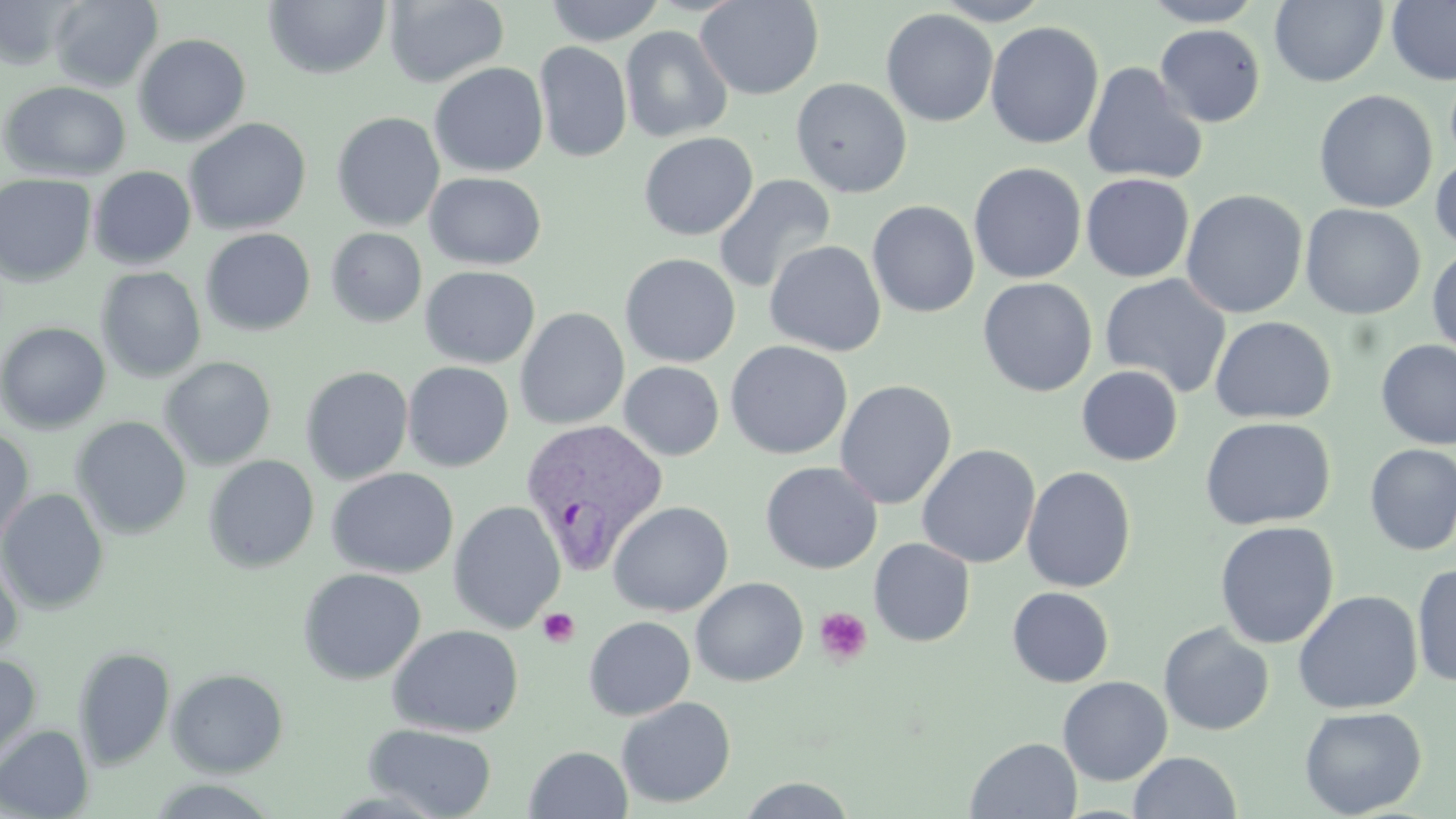
Summary:
  - Coordinate format: approximate bounding boxes as named x1/y1/x2/y2 corners in pixels
  - Plasmodium vivax-infected red blood cell locations: (x1=520, y1=418, x2=670, y2=574)
  - Uninfected red blood cell locations: (x1=49, y1=0, x2=163, y2=92), (x1=544, y1=0, x2=666, y2=46), (x1=694, y1=0, x2=824, y2=100), (x1=932, y1=0, x2=1052, y2=25), (x1=1140, y1=0, x2=1266, y2=26), (x1=1270, y1=0, x2=1388, y2=87), (x1=1386, y1=0, x2=1456, y2=86), (x1=0, y1=1, x2=80, y2=70), (x1=264, y1=1, x2=391, y2=79), (x1=384, y1=1, x2=509, y2=88), (x1=881, y1=8, x2=998, y2=127), (x1=985, y1=21, x2=1104, y2=150), (x1=981, y1=22, x2=1094, y2=285), (x1=1154, y1=24, x2=1266, y2=127), (x1=620, y1=25, x2=733, y2=143), (x1=133, y1=33, x2=252, y2=146), (x1=534, y1=41, x2=632, y2=162), (x1=1082, y1=61, x2=1208, y2=185), (x1=429, y1=62, x2=549, y2=177), (x1=790, y1=77, x2=912, y2=199), (x1=1, y1=80, x2=131, y2=182), (x1=1314, y1=89, x2=1437, y2=213), (x1=331, y1=112, x2=445, y2=232), (x1=184, y1=117, x2=312, y2=236), (x1=639, y1=132, x2=758, y2=240), (x1=1430, y1=151, x2=1456, y2=257), (x1=968, y1=162, x2=1087, y2=284), (x1=88, y1=166, x2=196, y2=270), (x1=0, y1=172, x2=97, y2=287), (x1=424, y1=172, x2=546, y2=270), (x1=1081, y1=172, x2=1194, y2=282), (x1=712, y1=174, x2=837, y2=294), (x1=1180, y1=189, x2=1308, y2=319), (x1=867, y1=200, x2=980, y2=317), (x1=1300, y1=203, x2=1426, y2=319), (x1=325, y1=227, x2=427, y2=327), (x1=201, y1=228, x2=316, y2=336), (x1=764, y1=240, x2=886, y2=357), (x1=1427, y1=245, x2=1456, y2=361), (x1=620, y1=253, x2=741, y2=368), (x1=420, y1=266, x2=540, y2=368), (x1=96, y1=267, x2=206, y2=382), (x1=1099, y1=274, x2=1231, y2=399), (x1=977, y1=278, x2=1097, y2=397), (x1=514, y1=307, x2=630, y2=430), (x1=1210, y1=315, x2=1336, y2=424), (x1=0, y1=321, x2=111, y2=434), (x1=1374, y1=339, x2=1456, y2=449), (x1=725, y1=340, x2=853, y2=460), (x1=158, y1=356, x2=277, y2=470), (x1=402, y1=361, x2=514, y2=472), (x1=619, y1=361, x2=725, y2=461), (x1=1076, y1=365, x2=1183, y2=466), (x1=300, y1=366, x2=413, y2=485), (x1=834, y1=380, x2=957, y2=509), (x1=71, y1=416, x2=192, y2=539), (x1=1199, y1=416, x2=1336, y2=531), (x1=0, y1=427, x2=34, y2=545), (x1=917, y1=444, x2=1040, y2=568), (x1=1364, y1=444, x2=1456, y2=556), (x1=203, y1=455, x2=319, y2=574), (x1=760, y1=461, x2=882, y2=574), (x1=1022, y1=466, x2=1137, y2=593), (x1=326, y1=467, x2=459, y2=579), (x1=0, y1=488, x2=109, y2=614), (x1=448, y1=501, x2=566, y2=634), (x1=608, y1=501, x2=733, y2=617), (x1=1215, y1=520, x2=1339, y2=650), (x1=869, y1=538, x2=976, y2=647), (x1=0, y1=548, x2=23, y2=663), (x1=1412, y1=562, x2=1456, y2=688), (x1=298, y1=567, x2=426, y2=685), (x1=690, y1=577, x2=809, y2=687), (x1=1007, y1=586, x2=1115, y2=688), (x1=1293, y1=589, x2=1423, y2=714), (x1=584, y1=616, x2=696, y2=720), (x1=1158, y1=622, x2=1274, y2=736), (x1=387, y1=624, x2=524, y2=737), (x1=73, y1=646, x2=176, y2=770), (x1=0, y1=654, x2=41, y2=764), (x1=167, y1=668, x2=289, y2=777), (x1=1058, y1=676, x2=1173, y2=785), (x1=616, y1=696, x2=736, y2=808), (x1=1299, y1=705, x2=1427, y2=818), (x1=364, y1=723, x2=498, y2=819), (x1=0, y1=724, x2=94, y2=818), (x1=965, y1=737, x2=1082, y2=818), (x1=524, y1=746, x2=633, y2=819), (x1=1128, y1=751, x2=1241, y2=819), (x1=145, y1=777, x2=283, y2=818), (x1=736, y1=777, x2=859, y2=818)
  - Platelet locations: (x1=814, y1=607, x2=872, y2=666), (x1=538, y1=608, x2=580, y2=647)
  - Slide-level diagnosis: Plasmodium vivax
  - Field of view: one of a larger specimen
  - Modality: light microscopy
  - Stain: May-Grünwald-Giemsa
  - Preparation: thin blood smear
  - Magnification: 1000x
  - Image size: 1456×819 pixels